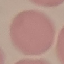

result = no malaria parasites detected
preparation = thin blood film
stain = Giemsa
capture = smartphone camera at the microscope eyepiece
image type = automatically extracted cell patch, resized to 64 × 64 pixels